Locate every Plasmodium parasite.
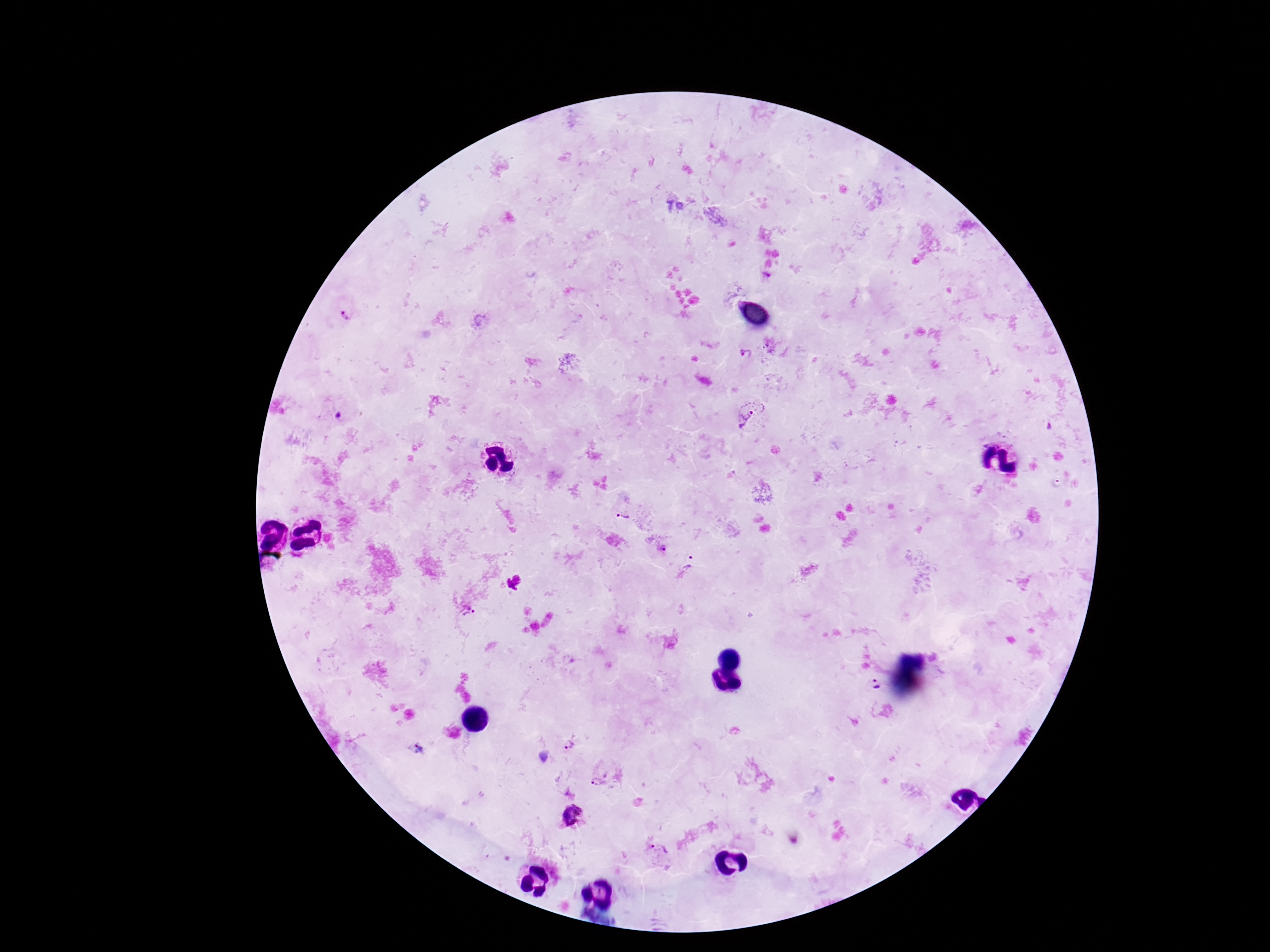

Approximate object centers, in pixels from the top-left corner.
Plasmodium parasites: (x=346, y=316), (x=746, y=354), (x=751, y=417), (x=623, y=515), (x=692, y=563), (x=467, y=613), (x=872, y=687), (x=416, y=748), (x=570, y=748), (x=602, y=776), (x=658, y=852).

Smartphone photograph taken through the microscope eyepiece. 100x magnification. Patient malaria status: infected. Image is 1270×952 pixels. Thick blood film. One field from this slide. Giemsa-stained preparation.